Classify this cell by malaria status.
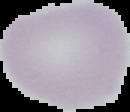

It is uninfected.

From a thin blood film. Image is 130×112 pixels. Segmented cell region on a black background.